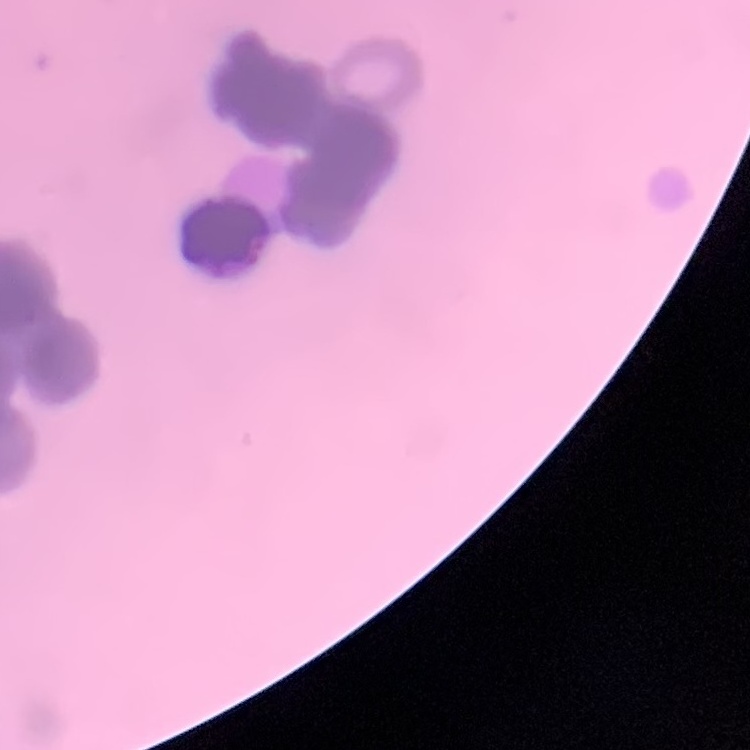

red blood cell morphology = rouleaux formation
preparation = thin blood film
image type = one tile cut from a larger photomicrograph
stain = Field's or Giemsa